Assess this cell for malaria.
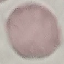

It is uninfected.

Summary:
  - Stain: Giemsa
  - Image type: cell patch, automatically extracted from a larger field of view and resized to 64 × 64 pixels
  - Capture: smartphone camera at the microscope eyepiece
  - Preparation: thin blood smear